Assess this cell for malaria.
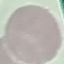

Uninfected.

Summary:
  - Preparation: thin smear
  - Stain: Giemsa
  - Capture: smartphone camera at the microscope eyepiece
  - Image type: cell patch, automatically extracted from a larger field of view and resized to 64 × 64 pixels